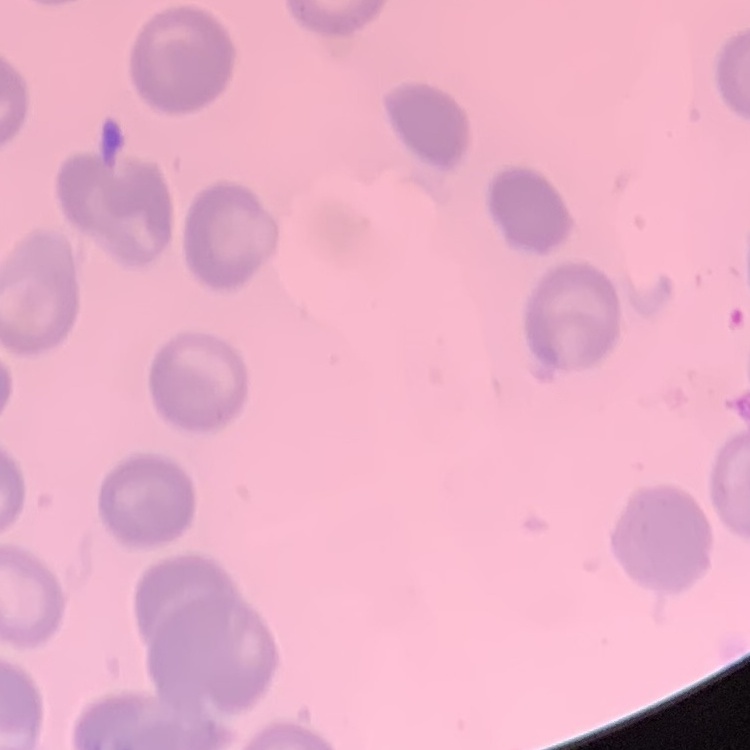

erythrocyte_morphology: no rouleaux formation
preparation: thin blood film
stain: Field's or Giemsa
image_type: square crop of a larger photomicrograph